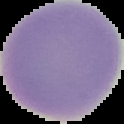 Malaria status: uninfected. Segmented cell region on a black background. From a thin blood film. Image is 124×124 pixels.